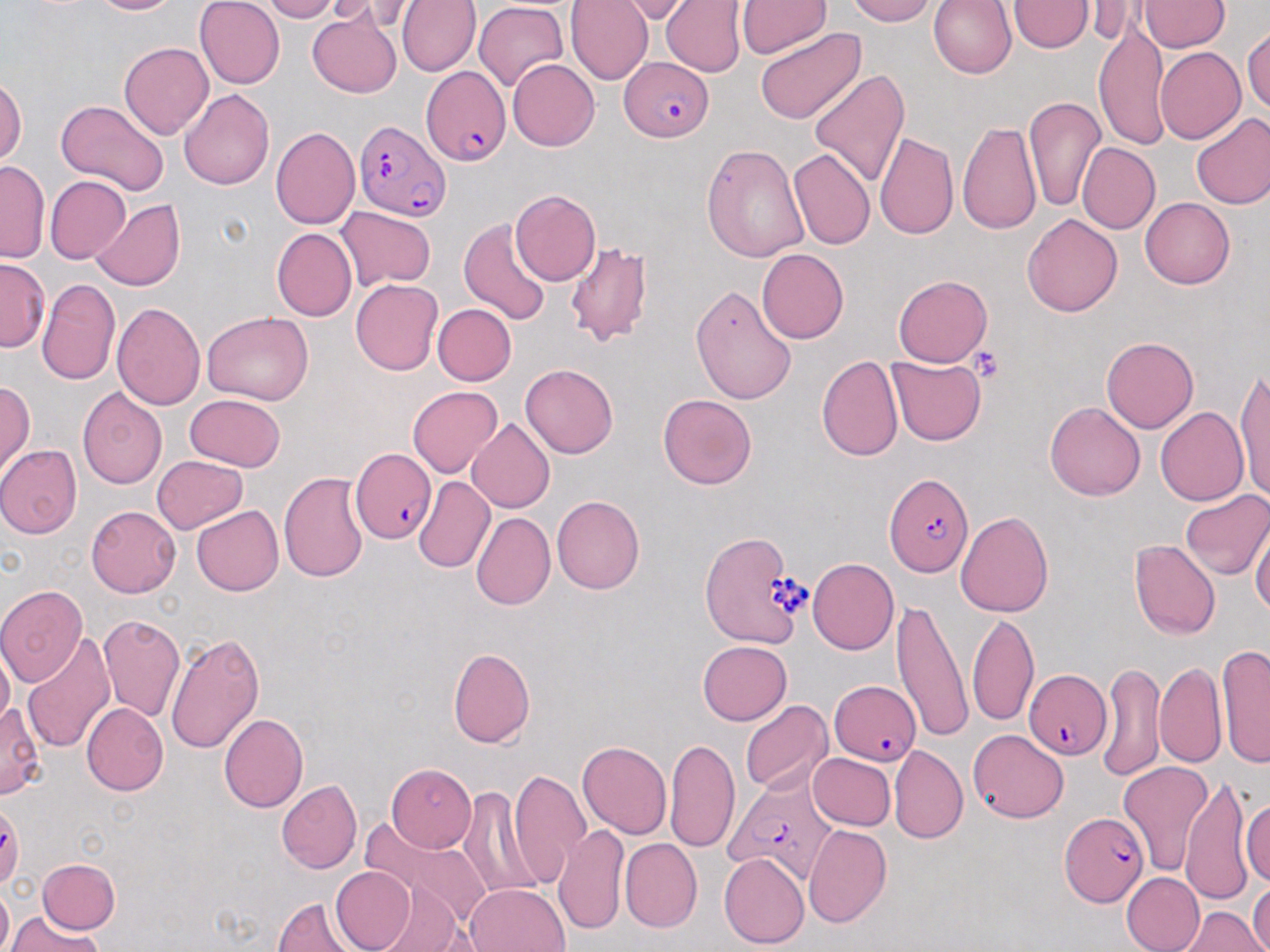
slide-level diagnosis = Plasmodium falciparum
uninfected red blood cell locations = approximate bounding boxes as (x1,y1)-(x2,y2) corner pairs in pixels: (87,0)-(184,17), (196,0)-(285,88), (257,0)-(340,22), (316,0)-(393,24), (397,0)-(478,75), (566,0)-(654,84), (619,0)-(694,21), (661,0)-(747,77), (738,0)-(829,58), (846,0)-(934,26), (929,0)-(1018,79), (1085,0)-(1140,45), (1141,0)-(1227,52), (1010,1)-(1090,53), (472,3)-(572,93), (307,11)-(402,95), (1095,25)-(1170,146), (1243,27)-(1270,119), (752,28)-(865,125), (119,42)-(213,140), (1153,44)-(1244,141), (508,58)-(600,150), (810,70)-(910,187), (0,78)-(24,171), (179,86)-(274,192), (1024,94)-(1104,211), (55,101)-(168,194), (1190,111)-(1270,210), (957,120)-(1042,233), (270,126)-(360,231), (873,130)-(959,244), (1076,142)-(1159,234), (701,143)-(808,261), (788,147)-(876,252), (0,161)-(46,261), (43,175)-(130,264), (510,190)-(599,284), (1140,196)-(1234,288), (91,198)-(183,290), (336,205)-(438,288), (1022,212)-(1123,319), (458,219)-(552,327), (270,227)-(355,322), (561,239)-(656,346), (755,248)-(848,345), (0,261)-(48,349), (894,275)-(993,366), (38,278)-(120,385), (352,279)-(443,375), (690,285)-(799,404), (114,300)-(209,409), (433,303)-(516,386), (202,311)-(313,407), (1101,335)-(1199,433), (818,354)-(904,464), (887,356)-(987,445), (519,363)-(619,459), (1235,367)-(1270,500), (0,382)-(35,475), (407,385)-(502,478), (76,389)-(168,492), (186,392)-(286,471), (658,394)-(757,489), (1046,399)-(1146,501), (1154,407)-(1248,507), (467,417)-(558,513), (0,445)-(80,537), (153,455)-(248,534), (277,469)-(371,585), (412,474)-(494,573), (1182,488)-(1269,583), (552,495)-(645,594), (86,505)-(181,598), (192,505)-(285,596), (955,509)-(1055,617), (471,513)-(554,611), (1251,517)-(1269,622), (1130,541)-(1219,639), (807,557)-(900,654), (0,585)-(90,683), (892,603)-(970,744), (967,611)-(1038,726), (98,615)-(185,724), (22,629)-(116,755), (165,629)-(267,752), (698,642)-(792,724), (1218,644)-(1270,767), (448,648)-(536,747), (1156,661)-(1225,766), (1097,663)-(1168,781), (0,698)-(45,798), (740,699)-(831,795), (83,703)-(168,793), (217,712)-(307,812), (968,729)-(1068,823), (665,740)-(740,854), (578,741)-(671,840), (891,746)-(967,842), (806,751)-(895,832), (1118,760)-(1212,876), (388,765)-(478,849), (509,768)-(591,891), (1180,775)-(1257,903), (277,779)-(362,874), (466,780)-(543,909), (1242,792)-(1270,887), (0,803)-(23,890), (370,814)-(499,927), (555,822)-(629,934), (803,825)-(892,928), (620,839)-(700,933), (721,852)-(808,948), (38,859)-(119,933), (328,865)-(417,951), (1121,873)-(1204,952), (1250,877)-(1269,952), (371,879)-(471,952), (464,882)-(570,952), (273,895)-(362,952), (1181,907)-(1265,952), (5,915)-(103,952)
image size = 1270×952 pixels
modality = optical microscopy
platelet locations = approximate bounding boxes as (x1,y1)-(x2,y2) corner pairs in pixels: (971,346)-(1004,380)
stain = May-Grünwald-Giemsa
magnification = 1000x
preparation = thin blood smear
Plasmodium falciparum-infected red blood cell locations = approximate bounding boxes as (x1,y1)-(x2,y2) corner pairs in pixels: (621,53)-(715,142), (418,69)-(511,165), (356,120)-(449,222), (349,448)-(434,546), (883,468)-(972,577), (701,530)-(810,650), (1022,667)-(1114,761), (827,681)-(922,765), (718,778)-(833,881), (1058,811)-(1149,906)
field of view = single